Describe the morphology of the red blood cells.
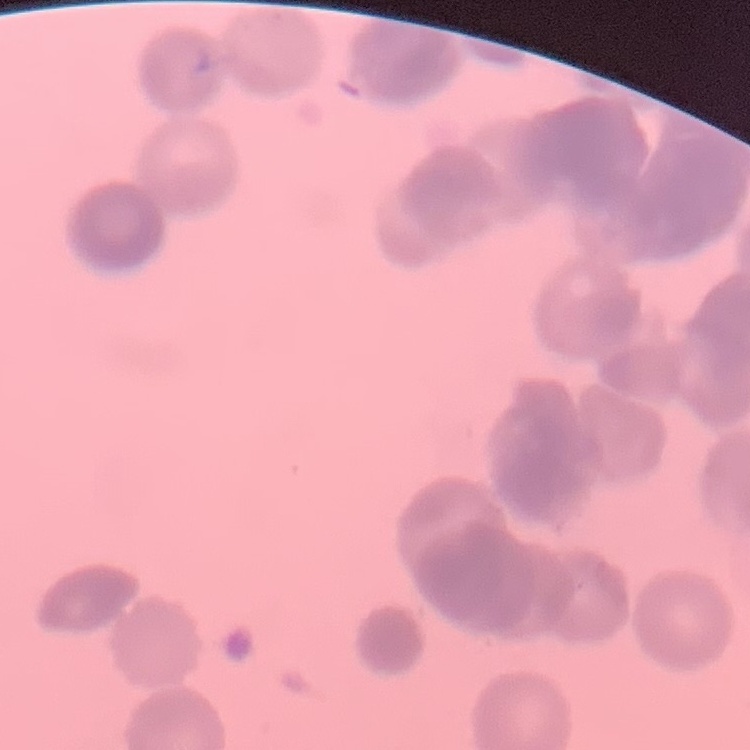

They show rouleaux formation.

Summary:
  - Image type: one tile cut from a larger photomicrograph
  - Preparation: thin peripheral smear
  - Stain: Field's or Giemsa